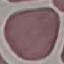
malaria status = uninfected
stain = Giemsa
preparation = thin blood smear
capture = smartphone through the microscope eyepiece
image type = automatically extracted cell patch, resized to 64 × 64 pixels